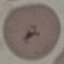
malaria status = uninfected
capture = smartphone through the microscope eyepiece
image type = cell patch, automatically extracted from a larger field of view and resized to 64 × 64 pixels
preparation = thin blood film
stain = Giemsa